Identify the parasite.
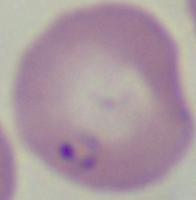
Babesia.

modality = micrograph
magnification = 1000x